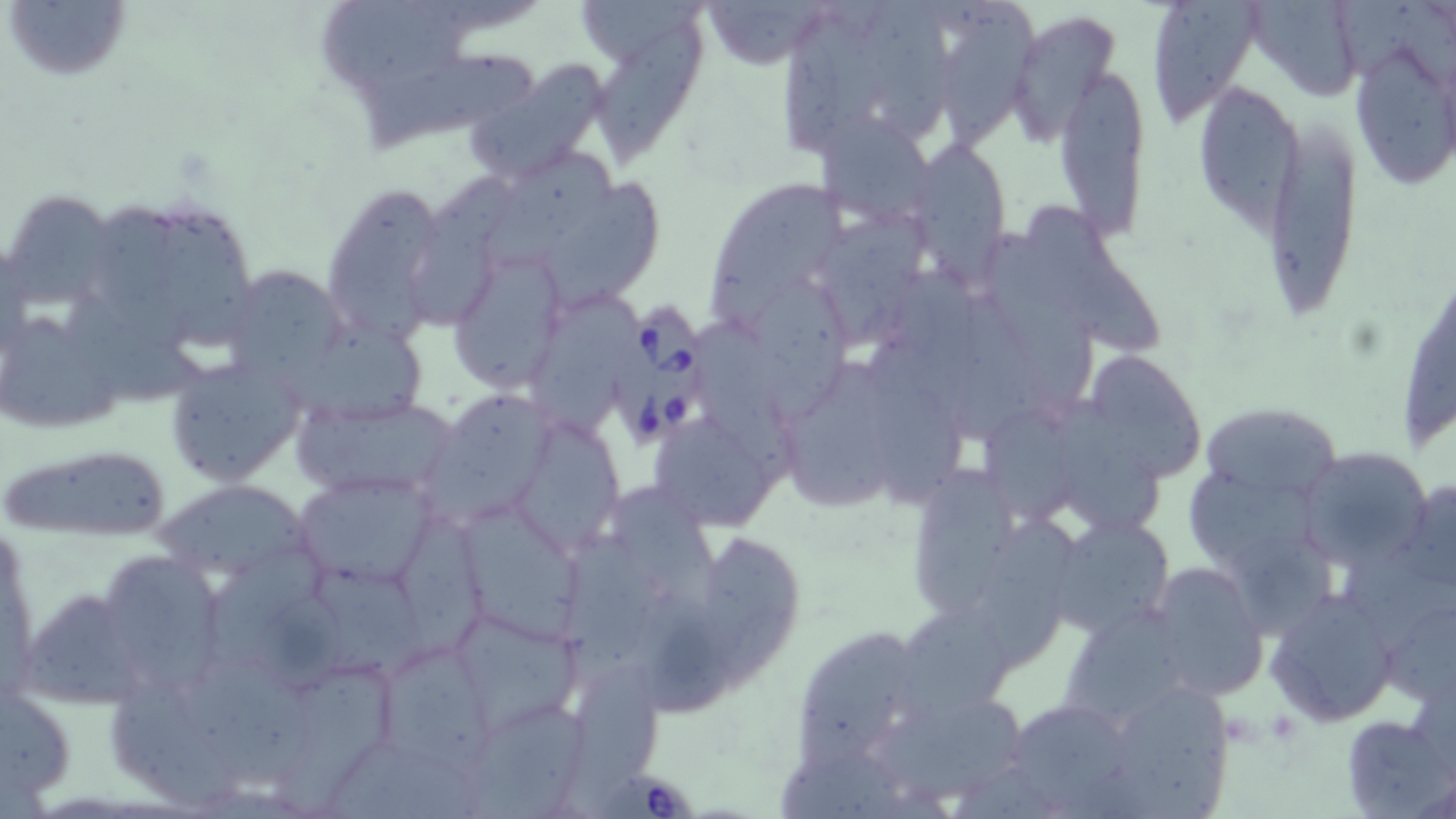
Summary:
  - Coordinate format: approximate bounding boxes as named x1/y1/x2/y2 corners in pixels
  - Uninfected red blood cell locations: (x1=5, y1=0, x2=132, y2=83), (x1=321, y1=0, x2=470, y2=106), (x1=580, y1=0, x2=706, y2=75), (x1=693, y1=0, x2=837, y2=69), (x1=788, y1=0, x2=885, y2=153), (x1=860, y1=0, x2=956, y2=143), (x1=944, y1=0, x2=1038, y2=156), (x1=1143, y1=0, x2=1266, y2=126), (x1=1256, y1=1, x2=1360, y2=107), (x1=1009, y1=11, x2=1121, y2=147), (x1=587, y1=23, x2=718, y2=170), (x1=1347, y1=35, x2=1456, y2=191), (x1=366, y1=50, x2=540, y2=153), (x1=465, y1=59, x2=613, y2=183), (x1=1054, y1=60, x2=1150, y2=239), (x1=1194, y1=80, x2=1303, y2=235), (x1=811, y1=111, x2=938, y2=229), (x1=1263, y1=111, x2=1366, y2=324), (x1=910, y1=143, x2=1011, y2=271), (x1=482, y1=146, x2=615, y2=266), (x1=411, y1=173, x2=526, y2=325), (x1=701, y1=176, x2=848, y2=330), (x1=543, y1=179, x2=668, y2=307), (x1=321, y1=182, x2=451, y2=344), (x1=0, y1=187, x2=120, y2=316), (x1=163, y1=201, x2=255, y2=347), (x1=96, y1=203, x2=188, y2=345), (x1=1025, y1=207, x2=1169, y2=356), (x1=819, y1=208, x2=938, y2=342), (x1=986, y1=230, x2=1099, y2=401), (x1=447, y1=246, x2=566, y2=391), (x1=891, y1=258, x2=982, y2=364), (x1=1397, y1=262, x2=1454, y2=460), (x1=233, y1=266, x2=340, y2=388), (x1=752, y1=273, x2=848, y2=427), (x1=66, y1=292, x2=205, y2=405), (x1=533, y1=293, x2=638, y2=438), (x1=958, y1=295, x2=1046, y2=442), (x1=0, y1=315, x2=125, y2=431), (x1=692, y1=318, x2=796, y2=479), (x1=308, y1=325, x2=425, y2=427), (x1=868, y1=336, x2=963, y2=500), (x1=1082, y1=350, x2=1207, y2=482), (x1=162, y1=352, x2=308, y2=487), (x1=784, y1=359, x2=897, y2=516), (x1=424, y1=391, x2=550, y2=526), (x1=289, y1=394, x2=462, y2=504), (x1=1059, y1=397, x2=1170, y2=536), (x1=1197, y1=400, x2=1342, y2=502), (x1=981, y1=403, x2=1084, y2=523), (x1=647, y1=409, x2=783, y2=530), (x1=518, y1=423, x2=621, y2=560), (x1=3, y1=442, x2=175, y2=542), (x1=1297, y1=447, x2=1432, y2=568), (x1=917, y1=464, x2=1013, y2=617), (x1=1180, y1=466, x2=1318, y2=567), (x1=294, y1=470, x2=440, y2=588), (x1=155, y1=475, x2=315, y2=578), (x1=1401, y1=476, x2=1456, y2=593), (x1=616, y1=486, x2=726, y2=604), (x1=466, y1=508, x2=586, y2=647), (x1=402, y1=512, x2=485, y2=660), (x1=1047, y1=513, x2=1177, y2=638), (x1=978, y1=519, x2=1076, y2=671), (x1=560, y1=533, x2=662, y2=679), (x1=704, y1=534, x2=807, y2=695), (x1=1222, y1=534, x2=1346, y2=640), (x1=211, y1=542, x2=327, y2=676), (x1=1347, y1=552, x2=1456, y2=651), (x1=107, y1=557, x2=226, y2=681), (x1=1146, y1=561, x2=1269, y2=703), (x1=315, y1=572, x2=426, y2=677), (x1=21, y1=588, x2=146, y2=712), (x1=638, y1=589, x2=745, y2=721), (x1=1267, y1=589, x2=1400, y2=728), (x1=1376, y1=595, x2=1456, y2=708), (x1=264, y1=598, x2=346, y2=692), (x1=892, y1=604, x2=1008, y2=728), (x1=1065, y1=607, x2=1184, y2=718), (x1=452, y1=610, x2=584, y2=734), (x1=797, y1=631, x2=921, y2=764), (x1=372, y1=637, x2=498, y2=771), (x1=186, y1=648, x2=302, y2=792), (x1=272, y1=664, x2=391, y2=818), (x1=559, y1=665, x2=662, y2=816), (x1=108, y1=672, x2=242, y2=806), (x1=1112, y1=682, x2=1230, y2=819), (x1=871, y1=686, x2=1033, y2=805), (x1=1, y1=689, x2=75, y2=810), (x1=1001, y1=695, x2=1141, y2=816), (x1=464, y1=702, x2=587, y2=819), (x1=1339, y1=713, x2=1453, y2=819), (x1=328, y1=740, x2=488, y2=819), (x1=774, y1=748, x2=914, y2=819)
  - Babesia divergens-infected red blood cell locations: (x1=616, y1=303, x2=712, y2=449), (x1=591, y1=771, x2=703, y2=819)
  - Slide-level diagnosis: Babesia divergens
  - Field of view: one of a larger specimen
  - Image size: 1456×819 pixels
  - Magnification: 1000x
  - Preparation: thin blood smear
  - Modality: light microscopy
  - Stain: May-Grünwald-Giemsa